Classify this cell by malaria status.
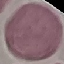
Uninfected.

Cell patch, automatically extracted from a larger field of view and resized to 64 × 64 pixels. Giemsa-stained preparation. Acquired by smartphone through the microscope eyepiece. Thin blood film.